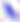

modality = micrograph
identification = Toxoplasma gondii
magnification = 400x